Comment on the morphology of the red blood cells.
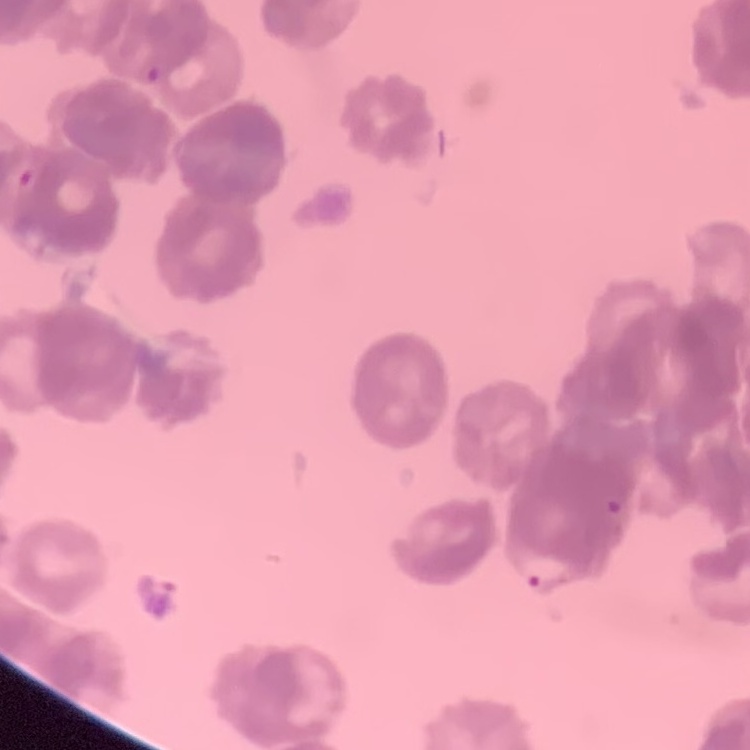
Rouleaux formation.

One tile cut from a larger photomicrograph. Field's or Giemsa stain. Thin blood smear.